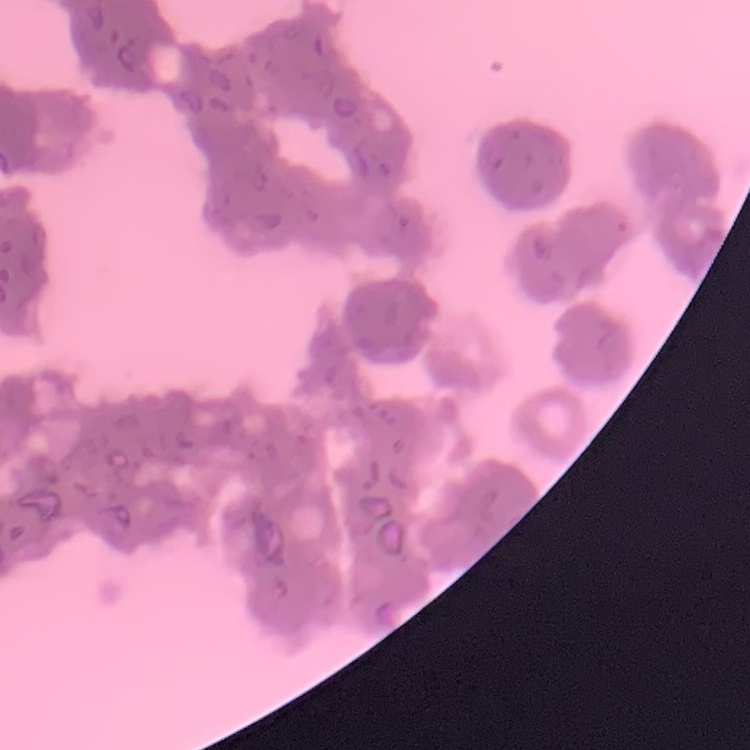
Summary:
  - Erythrocyte morphology: rouleaux formation
  - Image type: one tile cut from a larger photomicrograph
  - Stain: Field's or Giemsa
  - Preparation: thin blood smear